Classify this cell by malaria status.
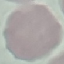

It is uninfected.

Summary:
  - Preparation: thin blood smear
  - Stain: Giemsa
  - Image type: automatically extracted cell patch, resized to 64 × 64 pixels
  - Capture: smartphone through the microscope eyepiece